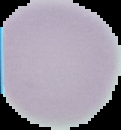

From a thin blood smear. Image is 121×130 pixels. Cell region segmented out of the field of view; the surrounding area is masked to black. Result: negative for Plasmodium parasites.